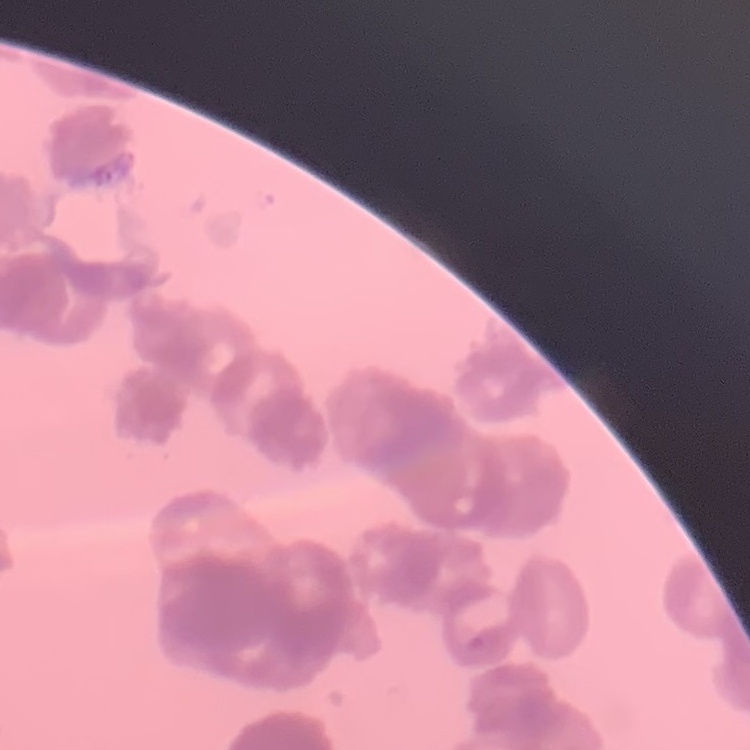
Summary:
  - Red blood cell morphology: rouleaux formation
  - Stain: Field's or Giemsa
  - Image type: square crop of a larger photomicrograph
  - Preparation: thin blood smear